Give the position of every Plasmodium parasite, noting whether each is a trophozoite, schizont, or gametocyte.
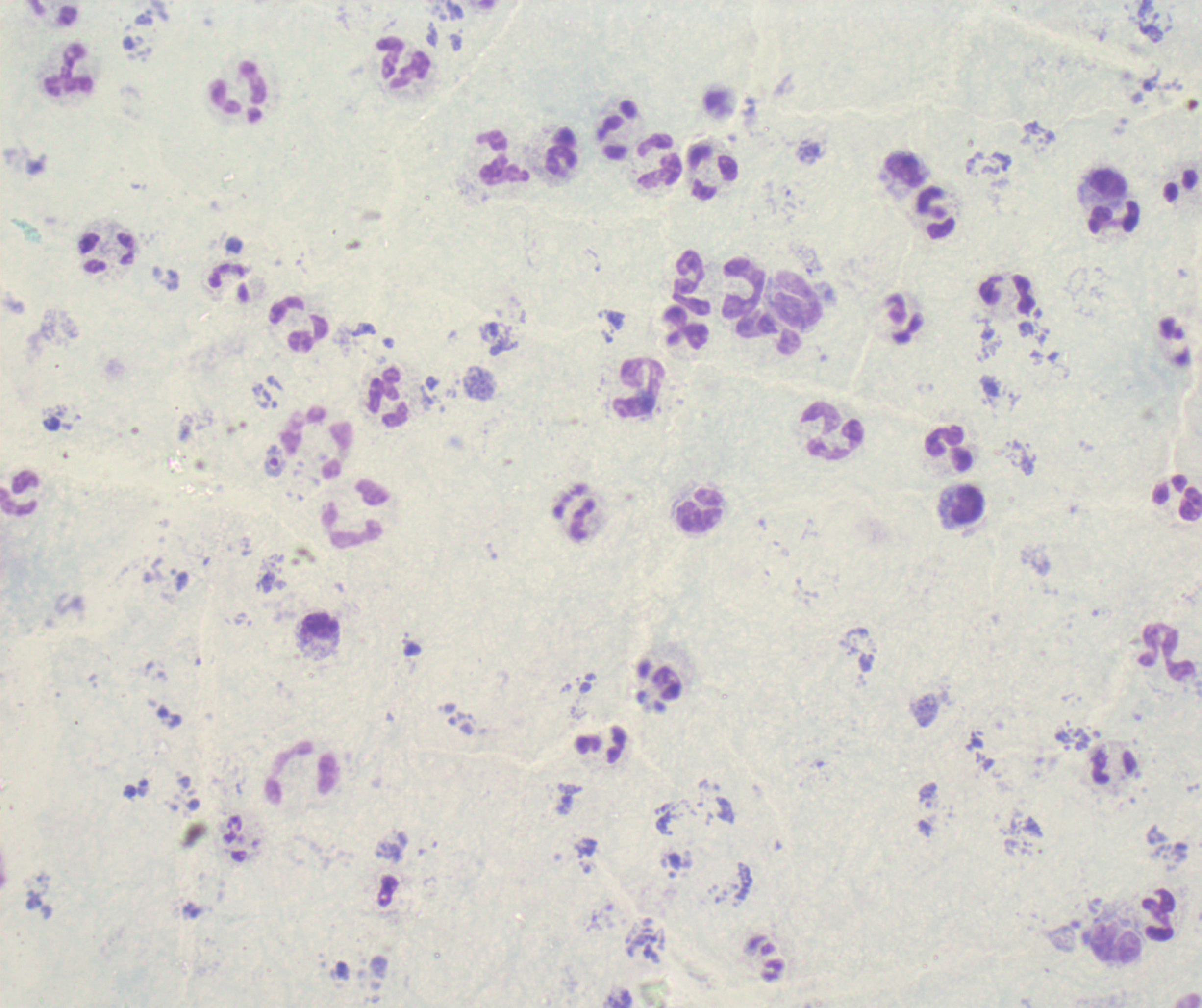

No Plasmodium parasites detected.

coordinate format = approximate object centers, in pixels from the top-left corner
leukocyte locations = (x=404, y=62), (x=70, y=71), (x=237, y=88), (x=617, y=129), (x=562, y=150), (x=502, y=159), (x=658, y=161), (x=904, y=172), (x=713, y=173), (x=1108, y=185), (x=935, y=212), (x=1114, y=219), (x=107, y=252), (x=693, y=283), (x=744, y=288), (x=1006, y=295), (x=798, y=301), (x=298, y=324), (x=685, y=327), (x=639, y=388), (x=389, y=398), (x=830, y=432), (x=319, y=443), (x=949, y=450), (x=20, y=493), (x=966, y=505), (x=575, y=511), (x=701, y=512), (x=353, y=514), (x=318, y=627), (x=1168, y=651), (x=1114, y=768), (x=301, y=773), (x=1158, y=915), (x=1117, y=943)
image size = 1202×1008 pixels
background quality = poor
context = previously used in a real diagnosis
preparation = thick blood film
magnification = 100x
stain = Romanowsky
field of view = one from this slide